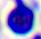

identification = leukocyte
modality = photomicrograph
magnification = 400x